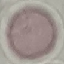
Summary:
  - Malaria status: uninfected
  - Stain: Giemsa
  - Image type: cell patch, automatically extracted from a larger field of view and resized to 64 × 64 pixels
  - Preparation: thin smear
  - Capture: smartphone through the microscope eyepiece